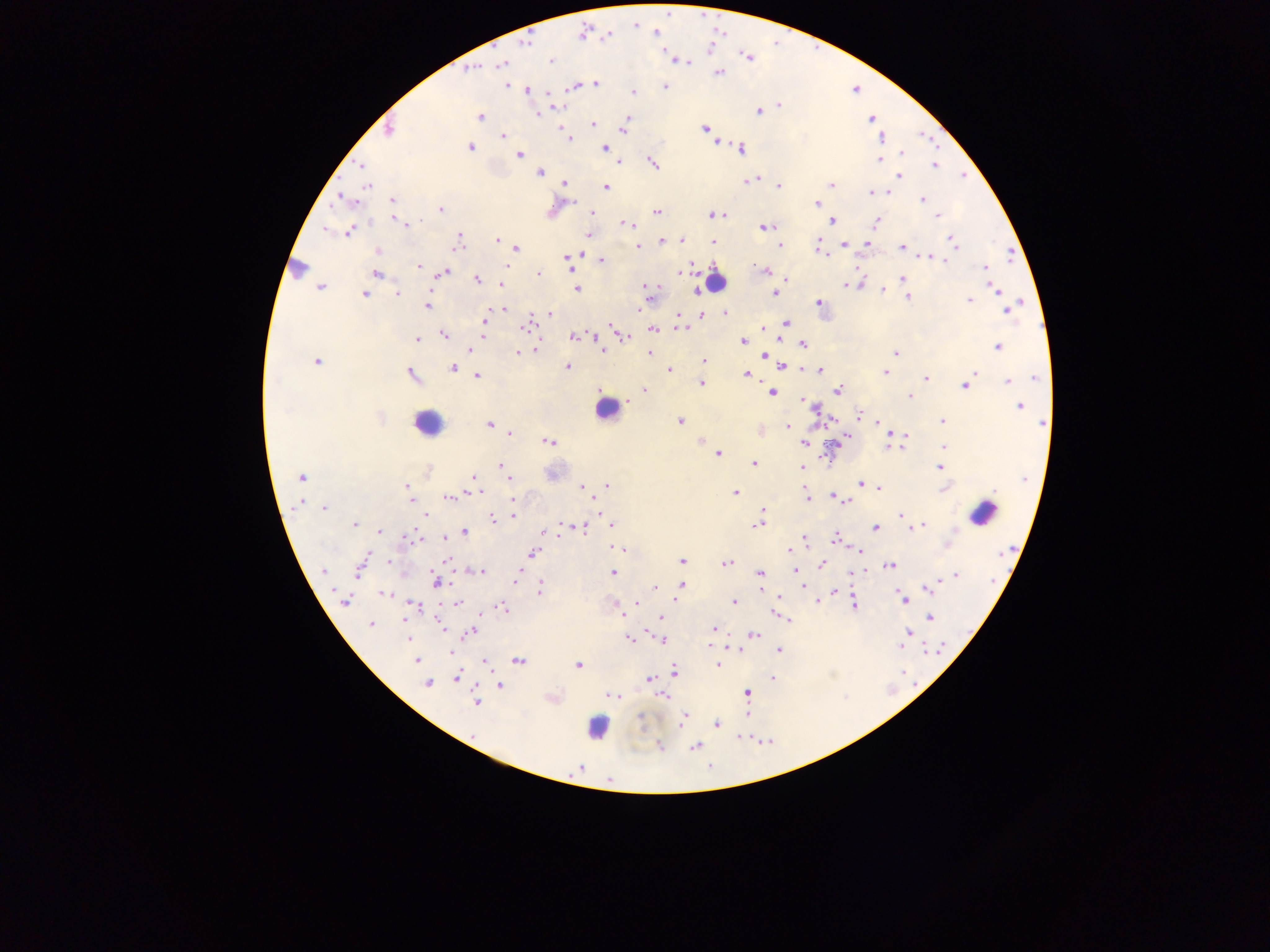
Approximate centers as x y in pixels.
Summary:
  - Malaria parasite locations: 656 33; 583 34; 607 35; 523 43; 669 57; 748 57; 676 59; 550 60; 687 61; 501 64; 471 69; 718 73; 595 83; 507 84; 574 85; 665 86; 527 90; 633 92; 549 94; 777 105; 554 107; 758 110; 536 115; 480 116; 628 117; 871 119; 592 125; 623 128; 705 129; 389 130; 503 136; 568 137; 882 137; 715 142; 604 147; 470 148; 740 149; 901 153; 519 154; 879 160; 617 162; 652 162; 362 165; 934 165; 539 171; 900 177; 747 180; 754 180; 564 183; 830 184; 366 186; 778 186; 605 187; 870 192; 885 192; 344 200; 922 200; 392 201; 817 203; 440 209; 657 211; 592 212; 725 214; 712 215; 938 216; 394 218; 831 220; 875 221; 400 222; 626 223; 408 225; 764 227; 327 228; 349 230; 588 235; 497 240; 680 240; 661 241; 712 241; 953 241; 867 242; 456 243; 818 243; 780 244; 844 244; 638 246; 902 247; 515 249; 378 251; 826 256; 930 257; 935 257; 567 258; 601 259; 418 265; 857 265; 506 266; 569 267; 985 267; 297 268; 766 271; 376 273; 443 273; 538 274; 678 274; 786 278; 477 279; 902 279; 501 283; 860 283; 845 284; 320 287; 646 287; 995 287; 576 289; 696 289; 883 290; 397 292; 648 293; 774 293; 364 294; 908 297; 970 299; 818 303; 427 305; 504 309; 1006 310; 725 312; 639 313; 550 314; 701 314; 677 316; 485 319; 785 322; 525 327; 613 328; 682 328; 762 328; 652 329; 444 334; 594 335; 483 336; 573 336; 625 337; 417 339; 743 341; 802 343; 996 346; 470 350; 535 350; 602 350; 518 352; 648 353; 895 353; 765 354; 316 360; 703 362; 782 366; 453 367; 566 367; 669 369; 803 369; 820 370; 885 372; 975 372; 410 374; 746 374; 477 375; 926 377; 1036 378; 1008 381; 701 383; 965 385; 645 391; 838 391; 771 392; 909 395; 629 400; 802 400; 808 405; 1018 406; 859 414; 830 420; 680 422; 877 422; 942 422; 1043 423; 488 424; 788 427; 759 430; 510 433; 898 433; 905 435; 700 440; 549 441; 804 442; 943 445; 887 446; 900 446; 716 454; 754 463; 501 465; 802 467; 939 467; 302 477; 473 478; 508 479; 859 483; 470 485; 586 486; 606 486; 866 486; 582 487; 407 488; 878 488; 943 488; 735 492; 469 493; 807 496; 831 496; 449 497; 512 497; 411 502; 846 502; 302 503; 596 507; 324 508; 599 511; 763 511; 425 515; 513 516; 761 516; 902 516; 491 518; 560 524; 756 524; 909 524; 354 525; 611 525; 924 525; 918 526; 580 528; 875 528; 380 531; 465 532; 543 533; 417 538; 443 538; 833 538; 805 539; 948 543; 619 548; 788 551; 857 551; 533 553; 446 560; 389 561; 682 561; 726 563; 361 565; 890 565; 821 566; 796 569; 323 571; 480 571; 760 572; 518 573; 613 573; 852 573; 956 576; 436 581; 515 581; 932 584; 682 585; 655 586; 928 588; 539 589; 760 590; 835 591; 383 593; 779 597; 903 598; 344 600; 817 601; 637 602; 734 602; 458 603; 413 605; 853 605; 501 608; 619 612; 774 612; 662 617; 929 618; 790 621; 438 622; 370 625; 442 627; 648 629; 713 629; 908 631; 469 632; 753 634; 408 638; 661 639; 630 640; 900 647; 738 648; 779 650; 449 651; 416 660; 518 660; 482 662; 717 664; 577 665; 673 670; 456 676; 772 677; 649 680; 427 683; 499 686; 746 693; 613 694; 663 696; 475 701; 747 714; 682 720; 716 724; 475 734; 695 746; 660 747; 580 768
  - Leukocyte locations: 716 279; 606 409; 427 423; 983 513; 598 727
  - Image size: 1270×952 pixels
  - Preparation: thick blood smear
  - Country: Ghana
  - Field of view: single
  - Capture: mobile-phone photograph through a microscope